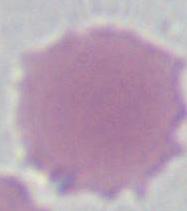

Summary:
  - Magnification: 1000x
  - Modality: photomicrograph
  - Identification: red blood cell